Report the malaria status of this cell.
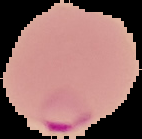
It is parasitized.

From a thin blood film. Image is 142×139 pixels. Segmented cell region on a black background.